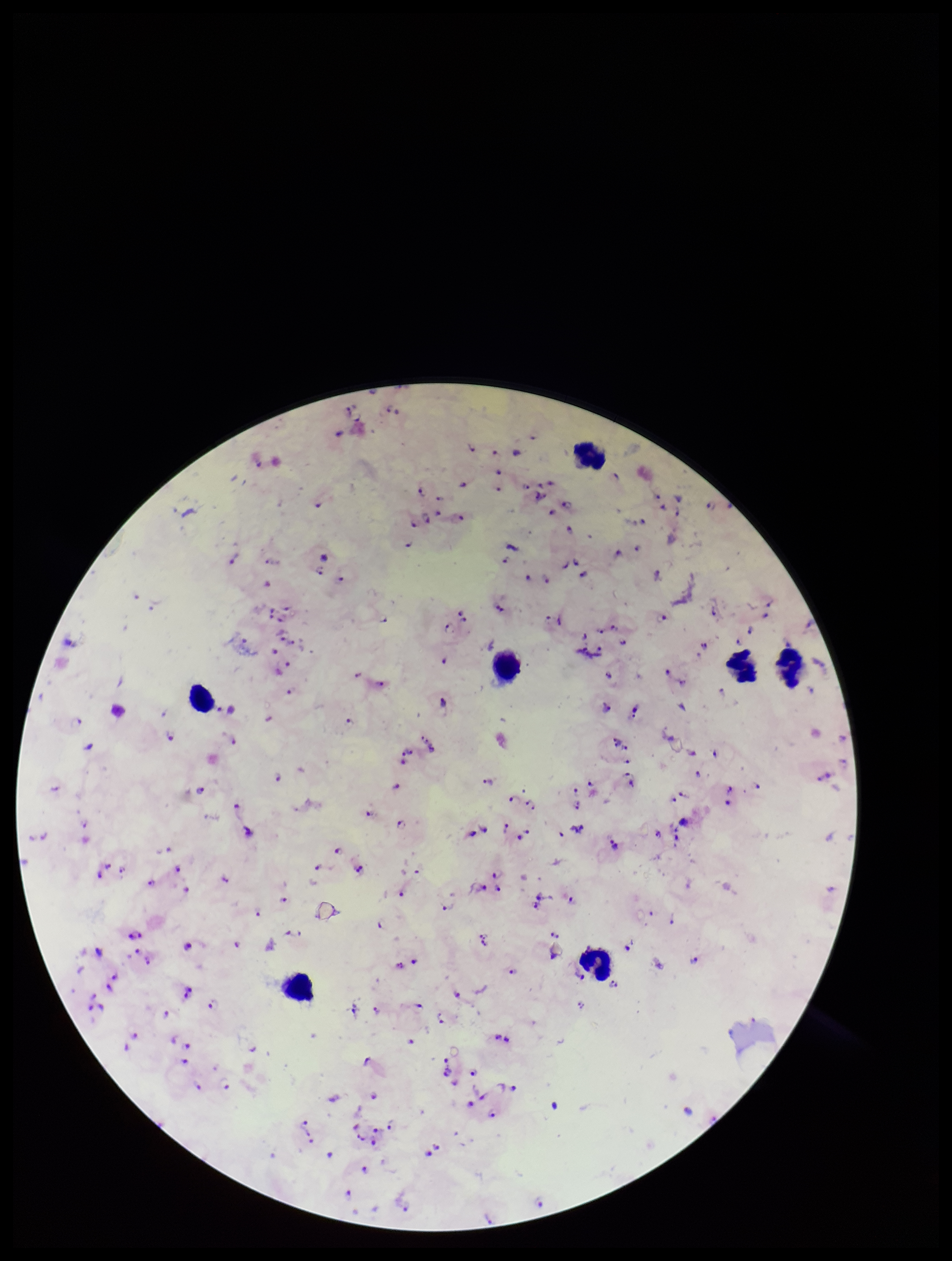
Species reported for this patient: Plasmodium falciparum. Image is 952×1261 pixels. Plasmodium parasites: identified. Parasite count: 119. Leukocyte count: 7. Smartphone photograph taken through the eyepiece of a microscope. Stained with Giemsa. Patient malaria status: infected. Preparation: thick smear. Single field of view.